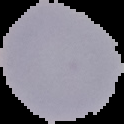

image type = segmented cell region on a black background
preparation = thin blood film
result = negative for Plasmodium parasites
image size = 124×124 pixels